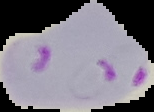

Summary:
  - Image size: 154×112 pixels
  - Preparation: thin blood smear
  - Image type: segmented cell region with the area outside set to black
  - Result: malaria parasites identified